Locate and identify every blood parasite.
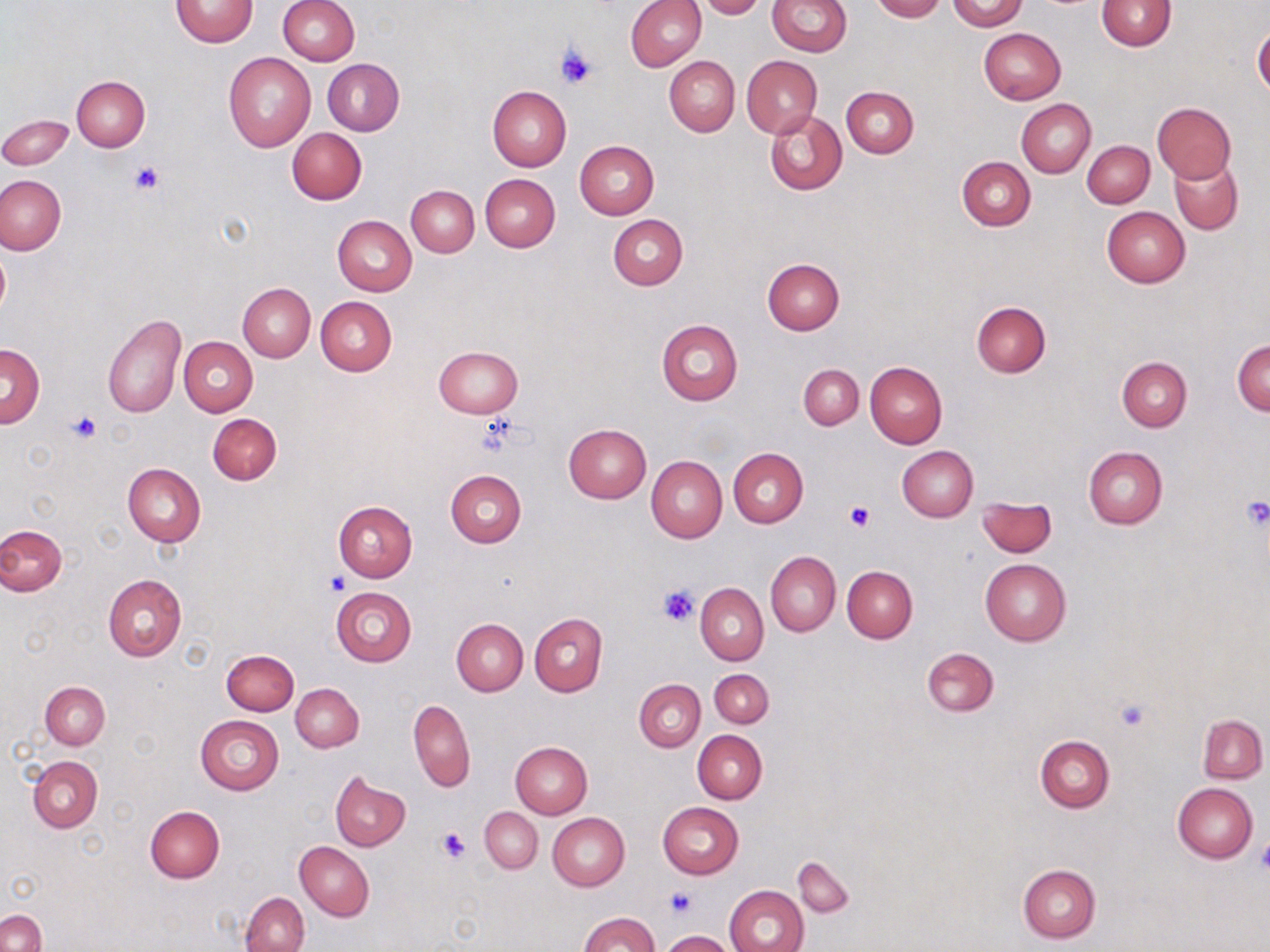
No blood parasites observed.

Summary:
  - Coordinate format: approximate bounding boxes as named x1/y1/x2/y2 corners in pixels
  - Platelet locations: (x1=555, y1=44, x2=598, y2=89), (x1=131, y1=162, x2=165, y2=194), (x1=66, y1=412, x2=101, y2=443), (x1=476, y1=414, x2=523, y2=456), (x1=1240, y1=497, x2=1270, y2=528), (x1=843, y1=502, x2=874, y2=532), (x1=324, y1=573, x2=350, y2=597), (x1=657, y1=584, x2=701, y2=626), (x1=1114, y1=698, x2=1150, y2=731), (x1=437, y1=827, x2=472, y2=863), (x1=1256, y1=838, x2=1270, y2=875), (x1=665, y1=886, x2=697, y2=917)
  - Uninfected red blood cell locations: (x1=278, y1=0, x2=359, y2=65), (x1=625, y1=0, x2=706, y2=71), (x1=696, y1=0, x2=766, y2=18), (x1=767, y1=0, x2=851, y2=57), (x1=872, y1=0, x2=945, y2=22), (x1=948, y1=0, x2=1027, y2=31), (x1=170, y1=1, x2=258, y2=47), (x1=1096, y1=1, x2=1176, y2=50), (x1=1253, y1=27, x2=1270, y2=99), (x1=978, y1=28, x2=1065, y2=105), (x1=223, y1=52, x2=316, y2=152), (x1=742, y1=55, x2=821, y2=137), (x1=665, y1=56, x2=740, y2=137), (x1=323, y1=58, x2=404, y2=135), (x1=72, y1=77, x2=149, y2=151), (x1=487, y1=85, x2=570, y2=172), (x1=841, y1=86, x2=918, y2=158), (x1=1016, y1=99, x2=1096, y2=177), (x1=1153, y1=102, x2=1236, y2=182), (x1=764, y1=109, x2=846, y2=196), (x1=0, y1=113, x2=73, y2=170), (x1=287, y1=127, x2=367, y2=203), (x1=1082, y1=140, x2=1154, y2=208), (x1=575, y1=141, x2=658, y2=219), (x1=957, y1=157, x2=1035, y2=231), (x1=1170, y1=157, x2=1243, y2=234), (x1=480, y1=174, x2=559, y2=251), (x1=0, y1=175, x2=65, y2=254), (x1=406, y1=185, x2=478, y2=255), (x1=1102, y1=207, x2=1190, y2=287), (x1=608, y1=214, x2=687, y2=290), (x1=333, y1=216, x2=416, y2=296), (x1=324, y1=217, x2=401, y2=374), (x1=0, y1=246, x2=10, y2=322), (x1=763, y1=258, x2=844, y2=335), (x1=238, y1=282, x2=315, y2=362), (x1=315, y1=297, x2=396, y2=376), (x1=971, y1=302, x2=1050, y2=377), (x1=102, y1=314, x2=186, y2=419), (x1=656, y1=318, x2=744, y2=405), (x1=179, y1=337, x2=257, y2=416), (x1=1232, y1=340, x2=1269, y2=416), (x1=0, y1=343, x2=44, y2=427), (x1=434, y1=346, x2=523, y2=417), (x1=1117, y1=356, x2=1192, y2=431), (x1=866, y1=362, x2=947, y2=448), (x1=798, y1=364, x2=863, y2=429), (x1=208, y1=412, x2=281, y2=485), (x1=563, y1=424, x2=650, y2=503), (x1=897, y1=446, x2=978, y2=522), (x1=1082, y1=446, x2=1167, y2=529), (x1=728, y1=447, x2=808, y2=528), (x1=647, y1=456, x2=727, y2=542), (x1=122, y1=462, x2=206, y2=546), (x1=446, y1=469, x2=526, y2=548), (x1=978, y1=497, x2=1056, y2=558), (x1=333, y1=501, x2=418, y2=581), (x1=0, y1=524, x2=66, y2=595), (x1=766, y1=551, x2=840, y2=635), (x1=980, y1=558, x2=1072, y2=646), (x1=842, y1=566, x2=917, y2=642), (x1=103, y1=574, x2=187, y2=661), (x1=692, y1=575, x2=832, y2=659), (x1=696, y1=583, x2=768, y2=664), (x1=331, y1=587, x2=417, y2=666), (x1=529, y1=612, x2=606, y2=696), (x1=451, y1=619, x2=527, y2=695), (x1=922, y1=647, x2=999, y2=717), (x1=221, y1=649, x2=298, y2=715), (x1=710, y1=669, x2=774, y2=727), (x1=635, y1=680, x2=705, y2=752), (x1=40, y1=682, x2=110, y2=750), (x1=291, y1=683, x2=363, y2=752), (x1=408, y1=698, x2=475, y2=791), (x1=1198, y1=714, x2=1267, y2=783), (x1=195, y1=715, x2=284, y2=795), (x1=693, y1=730, x2=766, y2=804), (x1=1035, y1=734, x2=1114, y2=811), (x1=510, y1=742, x2=592, y2=819), (x1=28, y1=756, x2=102, y2=831), (x1=329, y1=772, x2=410, y2=851), (x1=1172, y1=782, x2=1258, y2=862), (x1=658, y1=802, x2=743, y2=878), (x1=145, y1=806, x2=224, y2=882), (x1=479, y1=807, x2=542, y2=874), (x1=548, y1=814, x2=630, y2=891), (x1=295, y1=842, x2=374, y2=921), (x1=793, y1=857, x2=854, y2=917), (x1=1018, y1=864, x2=1100, y2=943), (x1=724, y1=885, x2=808, y2=952), (x1=242, y1=892, x2=309, y2=952), (x1=0, y1=911, x2=46, y2=952), (x1=579, y1=911, x2=660, y2=952), (x1=661, y1=931, x2=738, y2=952)
  - Slide-level diagnosis: no evidence of blood parasites
  - Stain: May-Grünwald-Giemsa
  - Image size: 1270×952 pixels
  - Magnification: 1000x
  - Modality: optical microscopy
  - Preparation: thin blood smear
  - Field of view: one of a larger specimen